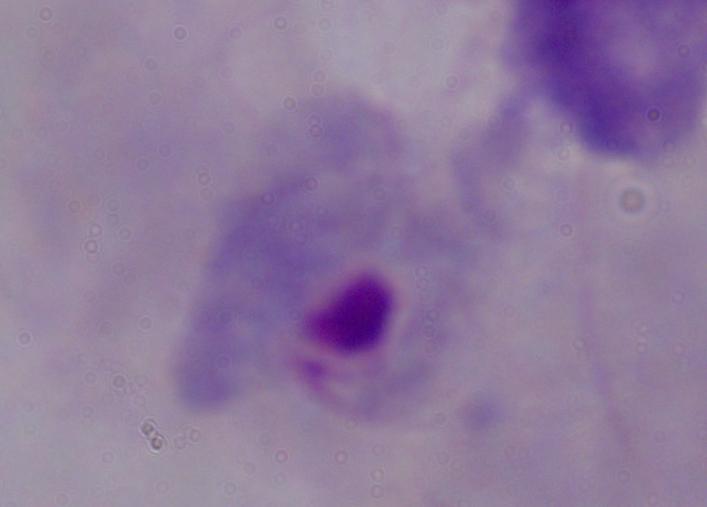 Captured at 1000x magnification. Micrograph. A trichomonad is shown.